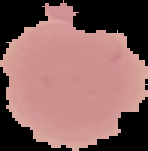
Summary:
  - Preparation: thin blood film
  - Image type: segmented cell region on a black background
  - Result: negative for Plasmodium parasites
  - Image size: 148×151 pixels